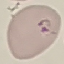
Summary:
  - Result: malaria parasites identified
  - Capture: smartphone through the microscope eyepiece
  - Preparation: thin blood film
  - Stain: Giemsa
  - Image type: automatically extracted cell patch, resized to 64 × 64 pixels